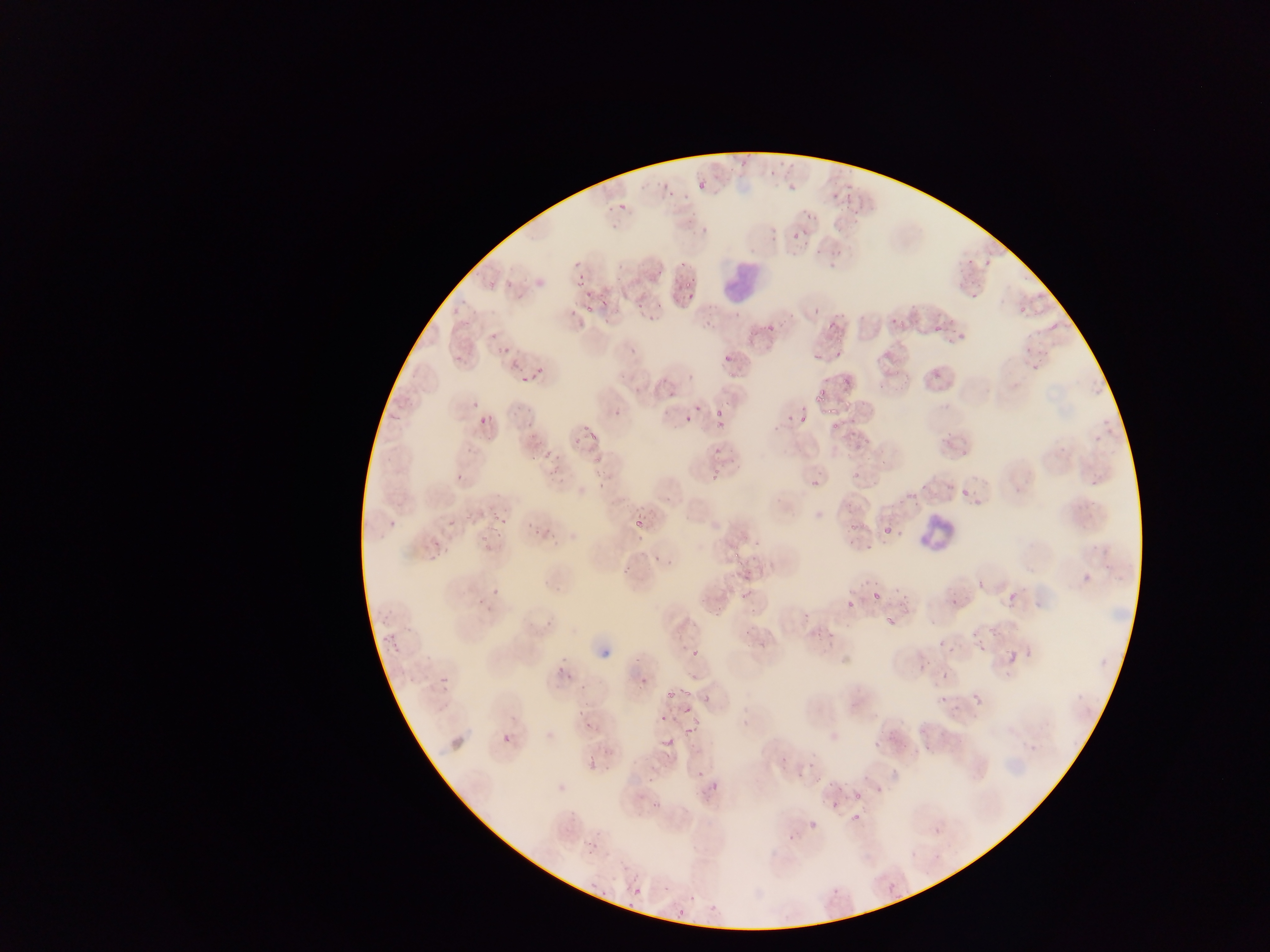

capture = mobile-phone photograph through a microscope
Plasmodium parasite locations = approximate bounding boxes as {left, top, right, bottom} in pixels: {737, 159, 748, 169}, {782, 161, 795, 169}, {726, 166, 734, 174}, {766, 169, 777, 178}, {654, 179, 667, 189}, {694, 179, 709, 192}, {784, 180, 797, 193}, {854, 181, 865, 220}, {829, 185, 840, 201}, {844, 185, 853, 211}, {668, 188, 677, 197}, {618, 202, 629, 212}, {798, 206, 812, 220}, {687, 212, 700, 221}, {698, 223, 711, 232}, {770, 223, 781, 233}, {791, 224, 809, 243}, {766, 237, 776, 244}, {828, 249, 844, 255}, {810, 251, 820, 258}, {963, 258, 975, 270}, {979, 260, 991, 268}, {677, 262, 690, 272}, {824, 263, 838, 270}, {575, 265, 592, 288}, {652, 269, 665, 277}, {682, 277, 694, 292}, {968, 291, 980, 301}, {580, 292, 592, 300}, {685, 293, 694, 301}, {601, 298, 611, 309}, {655, 298, 663, 312}, {1016, 298, 1031, 318}, {635, 300, 648, 312}, {704, 301, 722, 318}, {449, 302, 464, 316}, {584, 306, 591, 315}, {808, 307, 823, 316}, {833, 310, 845, 319}, {885, 312, 901, 325}, {648, 315, 658, 323}, {825, 319, 837, 329}, {764, 320, 779, 333}, {1050, 321, 1060, 330}, {700, 322, 713, 329}, {932, 325, 940, 332}, {744, 326, 758, 344}, {950, 330, 969, 345}, {489, 334, 498, 342}, {718, 344, 735, 371}, {1020, 345, 1036, 354}, {626, 346, 638, 354}, {494, 347, 511, 351}, {455, 352, 464, 360}, {812, 352, 823, 368}, {834, 352, 840, 360}, {505, 355, 517, 371}, {530, 360, 547, 377}, {1028, 362, 1043, 374}, {892, 363, 909, 377}, {932, 367, 946, 382}, {686, 370, 699, 383}, {517, 371, 527, 385}, {838, 376, 851, 388}, {815, 389, 826, 404}, {665, 390, 676, 400}, {470, 395, 489, 409}, {820, 401, 838, 413}, {693, 403, 701, 412}, {800, 404, 808, 414}, {711, 408, 723, 419}, {785, 409, 798, 420}, {608, 410, 620, 421}, {477, 412, 491, 425}, {684, 413, 694, 421}, {800, 414, 812, 428}, {832, 417, 840, 436}, {523, 418, 541, 428}, {770, 420, 783, 431}, {705, 422, 731, 428}, {585, 424, 604, 444}, {712, 444, 720, 455}, {556, 446, 566, 461}, {541, 448, 554, 461}, {548, 467, 561, 486}, {710, 467, 720, 482}, {852, 467, 864, 482}, {453, 475, 463, 485}, {808, 478, 823, 488}, {903, 485, 925, 502}, {959, 485, 968, 497}, {844, 503, 857, 514}, {490, 509, 507, 524}, {463, 512, 477, 521}, {388, 517, 402, 528}, {633, 517, 645, 531}, {448, 518, 459, 526}, {848, 520, 860, 533}, {528, 522, 540, 535}, {487, 527, 497, 532}, {883, 527, 891, 537}, {898, 529, 907, 540}, {544, 530, 560, 546}, {847, 534, 862, 546}, {482, 542, 500, 559}, {864, 543, 872, 552}, {426, 545, 443, 560}, {730, 552, 746, 568}, {649, 555, 661, 565}, {619, 566, 631, 578}, {976, 576, 990, 594}, {490, 583, 503, 598}, {890, 585, 908, 599}, {867, 587, 881, 601}, {1008, 589, 1022, 601}, {736, 592, 746, 605}, {841, 594, 855, 617}, {948, 597, 961, 606}, {482, 604, 496, 619}, {887, 610, 900, 624}, {801, 612, 810, 621}, {742, 627, 750, 637}, {378, 635, 402, 656}, {935, 639, 947, 647}, {976, 639, 993, 653}, {945, 641, 955, 657}, {1007, 649, 1019, 662}, {691, 651, 702, 663}, {551, 657, 568, 684}, {913, 661, 927, 675}, {937, 667, 952, 683}, {437, 671, 453, 683}, {639, 673, 649, 685}, {687, 673, 700, 682}, {579, 679, 594, 693}, {962, 682, 983, 708}, {665, 687, 677, 700}, {678, 687, 693, 694}, {704, 693, 711, 704}, {938, 693, 946, 704}, {953, 704, 960, 716}, {681, 708, 695, 722}, {575, 710, 590, 716}, {659, 714, 668, 722}, {584, 720, 602, 734}, {685, 724, 696, 737}, {501, 734, 512, 744}, {661, 735, 675, 749}, {872, 740, 883, 748}, {603, 746, 612, 754}, {586, 759, 596, 769}, {603, 760, 616, 771}, {779, 760, 789, 766}, {805, 763, 820, 770}, {794, 768, 809, 784}, {691, 769, 706, 780}, {710, 772, 722, 792}, {645, 774, 655, 785}, {823, 779, 838, 796}, {871, 785, 882, 795}, {697, 790, 709, 802}, {854, 790, 862, 802}, {649, 800, 667, 811}, {831, 801, 840, 810}, {849, 813, 860, 824}, {807, 816, 820, 832}, {933, 826, 941, 835}, {786, 835, 797, 843}, {586, 842, 599, 859}, {589, 882, 599, 890}, {887, 883, 894, 892}, {664, 885, 673, 892}, {629, 886, 645, 899}, {602, 889, 614, 906}, {687, 890, 697, 905}, {707, 896, 721, 917}, {625, 897, 635, 910}, {676, 906, 685, 919}
image size = 1270×952 pixels
preparation = thin blood smear
field of view = single
country = Ghana
leukocyte locations = approximate bounding boxes as {left, top, right, bottom} in pixels: {719, 255, 769, 302}, {913, 509, 960, 556}